Outline each uninfected red blood cell.
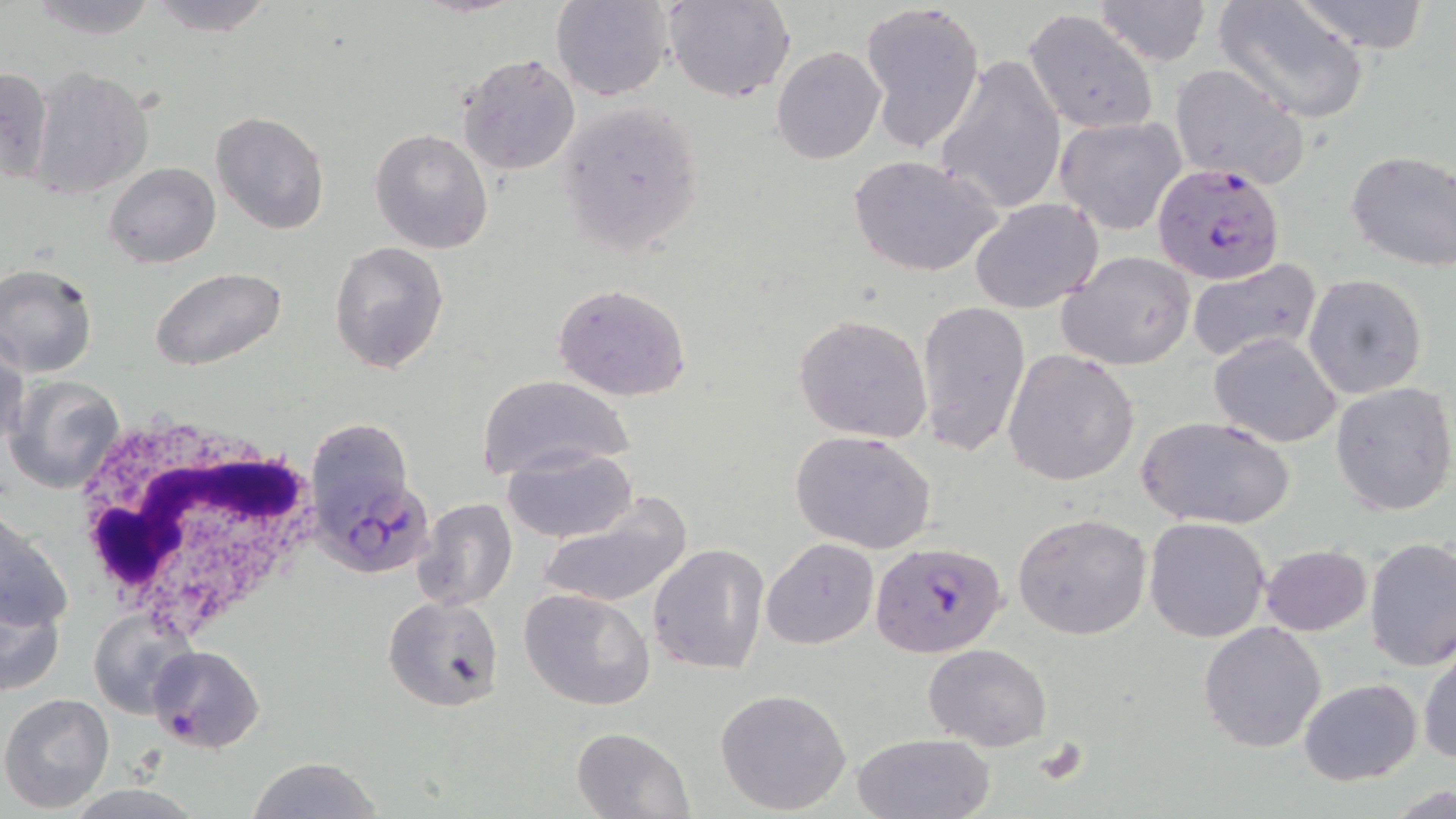
Approximate bounding boxes as [x1, y1, x2, y2] in pixels.
Uninfected red blood cells: [26, 0, 163, 42], [143, 0, 276, 35], [551, 0, 673, 101], [663, 0, 795, 104], [1288, 0, 1437, 53], [860, 2, 986, 152], [1092, 2, 1211, 65], [1215, 3, 1370, 122], [1023, 10, 1160, 134], [772, 46, 887, 164], [457, 53, 581, 175], [935, 53, 1066, 215], [1168, 62, 1311, 190], [0, 67, 53, 186], [28, 69, 151, 199], [556, 100, 706, 263], [211, 112, 330, 235], [1053, 117, 1186, 235], [369, 128, 494, 255], [1345, 149, 1456, 271], [850, 155, 1005, 278], [103, 161, 220, 268], [970, 198, 1103, 314], [329, 240, 450, 374], [1057, 251, 1196, 371], [1185, 259, 1322, 363], [0, 263, 100, 377], [147, 265, 288, 371], [1303, 274, 1428, 398], [552, 282, 694, 403], [915, 299, 1032, 457], [792, 313, 934, 444], [1208, 332, 1342, 448], [1, 341, 27, 455], [1003, 349, 1140, 486], [477, 374, 633, 483], [3, 375, 126, 495], [1330, 382, 1456, 517], [314, 416, 417, 513], [1136, 416, 1297, 529], [789, 429, 937, 554], [500, 447, 637, 543], [539, 493, 691, 612], [413, 498, 518, 615], [1, 509, 73, 640], [1012, 513, 1153, 641], [1143, 517, 1271, 642], [1364, 537, 1456, 671], [762, 538, 880, 650], [648, 543, 770, 676], [1260, 544, 1373, 636], [1, 584, 67, 701], [519, 588, 656, 713], [383, 596, 505, 712], [90, 607, 195, 714], [1197, 622, 1328, 753], [1417, 637, 1456, 768], [924, 643, 1052, 751], [1298, 679, 1421, 786], [715, 687, 853, 814], [0, 692, 115, 813], [571, 727, 694, 819], [852, 732, 995, 819], [245, 757, 387, 818].

slide-level diagnosis = Plasmodium falciparum
modality = light microscopy
white blood cell locations = approximate bounding boxes as [x1, y1, x2, y2] in pixels: [69, 411, 329, 638]
stain = May-Grünwald-Giemsa
image size = 1456×819 pixels
preparation = thin blood smear
Plasmodium falciparum-infected red blood cell locations = approximate bounding boxes as [x1, y1, x2, y2] in pixels: [1152, 162, 1286, 285], [331, 473, 438, 586], [870, 541, 1007, 658], [148, 644, 266, 752]
field of view = one of a larger specimen
magnification = 1000x